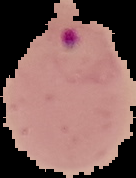

Image is 136×178 pixels. From a thin blood film. Segmented cell region on a black background. Result: malaria parasites detected.